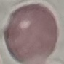
result = no malaria parasites seen
capture = smartphone through the microscope eyepiece
stain = Giemsa
preparation = thin blood smear
image type = cell patch, automatically extracted from a larger field of view and resized to 64 × 64 pixels